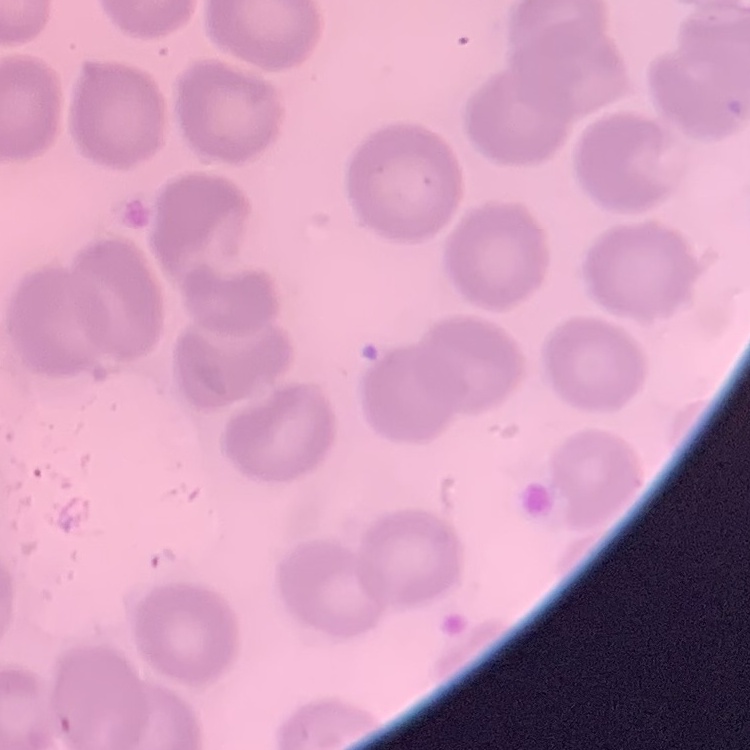

Summary:
  - Red blood cell morphology: no rouleaux formation
  - Preparation: thin blood smear
  - Stain: Field's or Giemsa
  - Image type: square crop of a larger photomicrograph